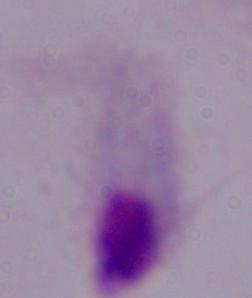

Summary:
  - Magnification: 1000x
  - Identification: trichomonad
  - Modality: micrograph